Classify this cell by malaria status.
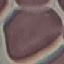

Uninfected.

Summary:
  - Preparation: thin smear
  - Stain: Giemsa
  - Image type: cell patch, automatically extracted from a larger field of view and resized to 64 × 64 pixels
  - Capture: smartphone through the microscope eyepiece